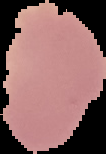

Summary:
  - Preparation: thin blood film
  - Image type: cell region segmented out of the field of view; surrounding area masked to black
  - Result: no malaria parasites detected
  - Image size: 106×154 pixels